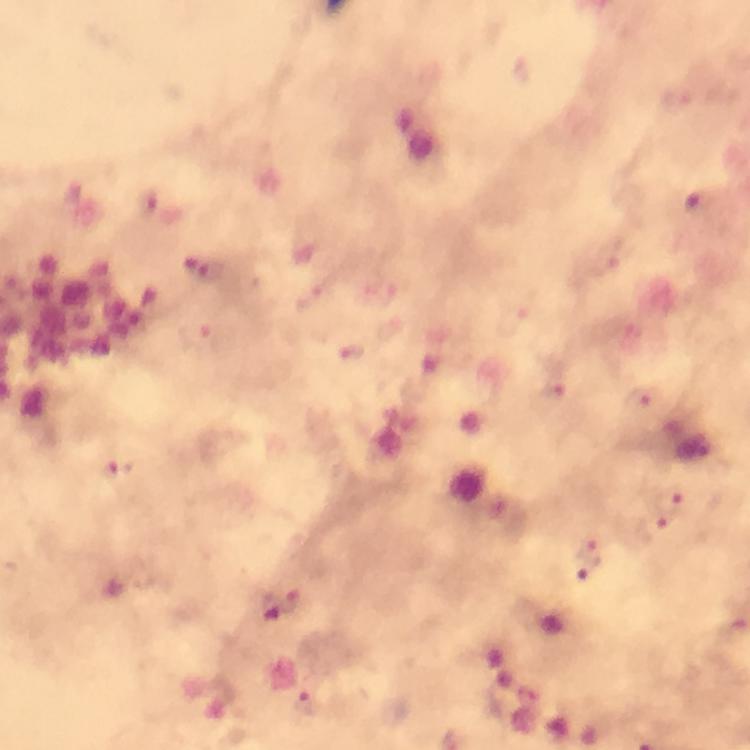
Approximate centers as (x, y) in pixels. Plasmodium parasite locations: (350, 353), (553, 391), (642, 397), (111, 472), (675, 497), (658, 525), (590, 554), (289, 599), (305, 702). A crop from one field of view. Image is 750×750 pixels. Giemsa stain. Thick blood smear. From a diagnostic examination for malaria. Photographed with a smartphone mounted on the microscope. Immersion oil was used. 100x magnification.